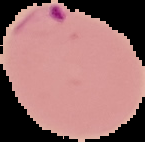

Segmented cell region on a black background. Image is 145×142 pixels. From a thin blood smear. Malaria status: parasitized.